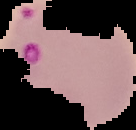
Summary:
  - Image type: segmented cell region with the area outside set to black
  - Image size: 136×130 pixels
  - Result: Plasmodium parasites identified
  - Preparation: thin blood film